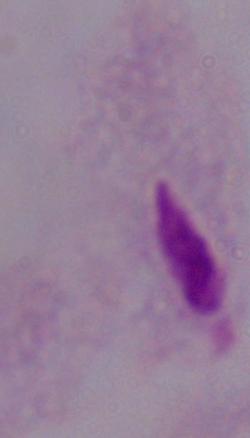

Summary:
  - Magnification: 1000x
  - Identification: trichomonad
  - Modality: photomicrograph